Describe the morphology of the erythrocytes.
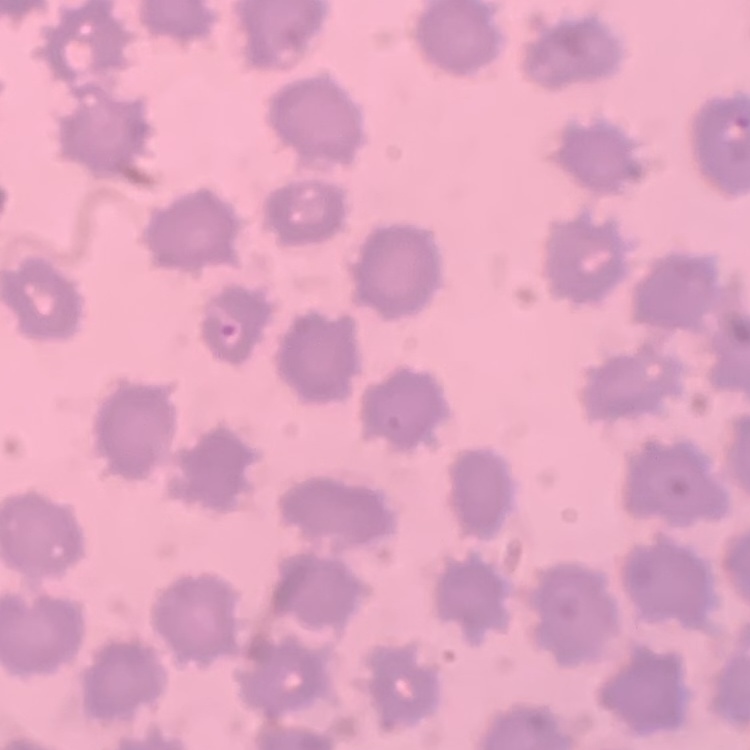

No rouleaux formation.

Summary:
  - Stain: Field's or Giemsa
  - Preparation: thin blood film
  - Image type: square crop of a larger photomicrograph